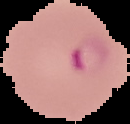
result = Plasmodium parasites identified
image type = segmented cell region with the area outside set to black
preparation = thin blood film
image size = 130×124 pixels